Locate every leukocyte (white blood cell).
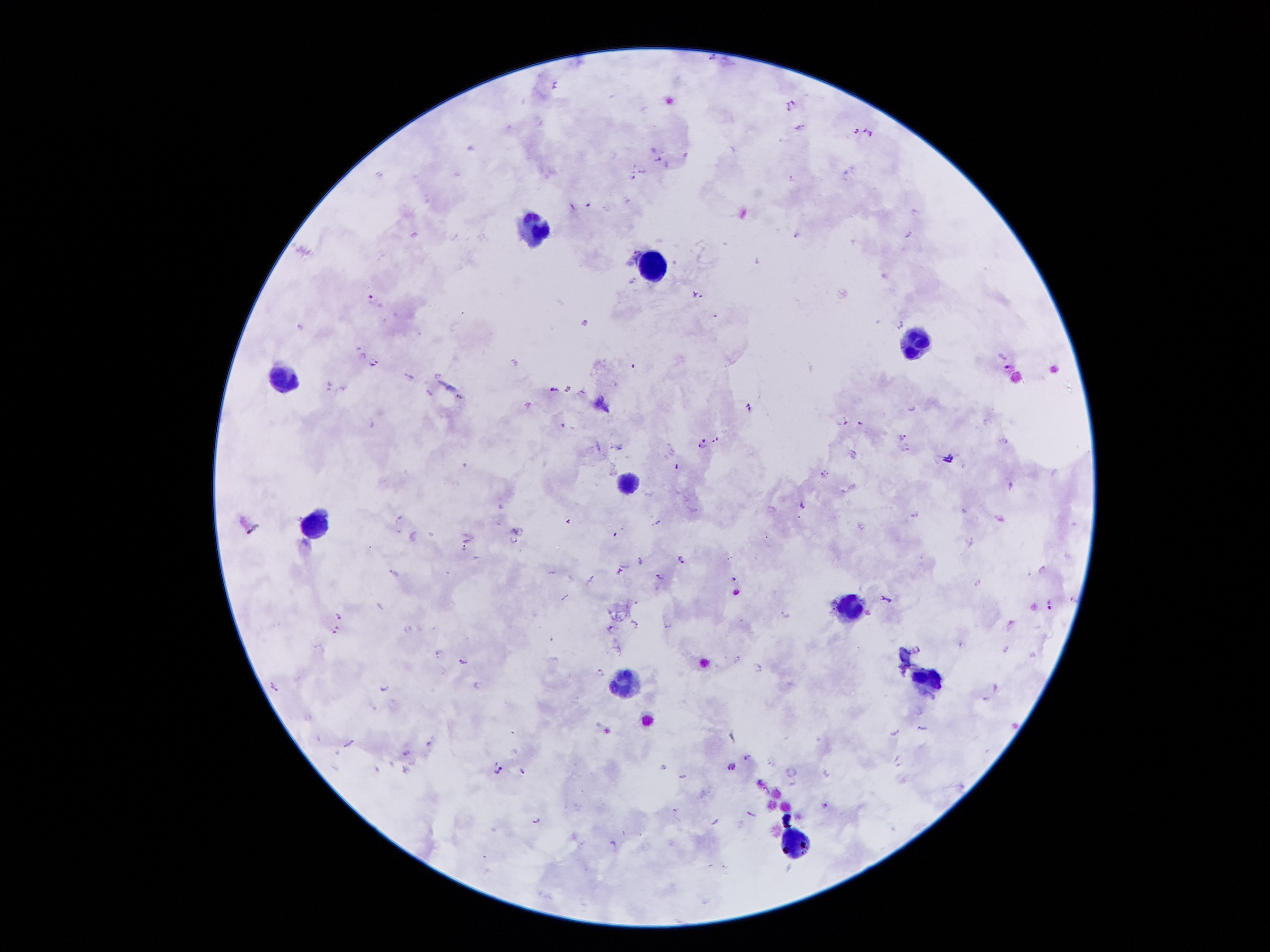

Approximate object centers, in pixels from the top-left corner.
Leukocytes: (x=533, y=228), (x=651, y=264), (x=917, y=344), (x=280, y=373), (x=628, y=483), (x=316, y=525), (x=845, y=609), (x=628, y=681), (x=929, y=683), (x=794, y=841).

magnification: 100x
stain: Giemsa
preparation: thick peripheral-blood smear
malaria_parasite_locations: 'approximate object centers, in pixels from the top-left corner: (x=710, y=57), (x=710, y=58), (x=554, y=83), (x=789, y=101), (x=792, y=102), (x=788, y=108), (x=800, y=125), (x=855, y=126), (x=857, y=129), (x=870, y=130), (x=657, y=156), (x=657, y=158), (x=639, y=169), (x=640, y=171), (x=790, y=176), (x=633, y=177), (x=572, y=207), (x=913, y=208), (x=907, y=232), (x=793, y=234), (x=633, y=250), (x=632, y=280), (x=694, y=291), (x=367, y=293), (x=701, y=295), (x=716, y=315), (x=585, y=322), (x=898, y=324), (x=300, y=325), (x=363, y=353), (x=514, y=359), (x=373, y=363), (x=1006, y=364), (x=406, y=374), (x=329, y=384), (x=551, y=387), (x=581, y=390), (x=528, y=405), (x=749, y=406), (x=843, y=419), (x=858, y=422), (x=562, y=424), (x=901, y=433), (x=715, y=437), (x=702, y=439), (x=1004, y=439), (x=699, y=445), (x=907, y=449), (x=670, y=450), (x=854, y=450), (x=665, y=457), (x=821, y=472), (x=1010, y=484), (x=799, y=505), (x=911, y=514), (x=399, y=517), (x=656, y=520), (x=512, y=537), (x=971, y=542), (x=461, y=544), (x=681, y=559), (x=617, y=567), (x=1043, y=567), (x=389, y=568), (x=659, y=575), (x=733, y=578), (x=977, y=581), (x=889, y=598), (x=1047, y=601), (x=784, y=614), (x=335, y=615), (x=633, y=622), (x=1010, y=622), (x=666, y=626), (x=609, y=628), (x=409, y=629), (x=334, y=630), (x=916, y=647), (x=1005, y=647), (x=435, y=652), (x=736, y=653), (x=462, y=663), (x=757, y=666), (x=597, y=668), (x=275, y=686), (x=380, y=687), (x=995, y=687), (x=983, y=698), (x=918, y=727), (x=893, y=729), (x=348, y=741), (x=427, y=743), (x=405, y=754), (x=744, y=756), (x=896, y=761), (x=662, y=764), (x=730, y=764), (x=494, y=766), (x=403, y=768), (x=790, y=769), (x=523, y=772), (x=680, y=775), (x=826, y=804), (x=674, y=810), (x=751, y=812), (x=534, y=818), (x=716, y=822), (x=612, y=842)'
field_of_view: single
capture: smartphone through the microscope eyepiece
image_size: 1270×952 pixels
patient_malaria_status: positive for Plasmodium falciparum